Locate every Plasmodium falciparum-infected red blood cell.
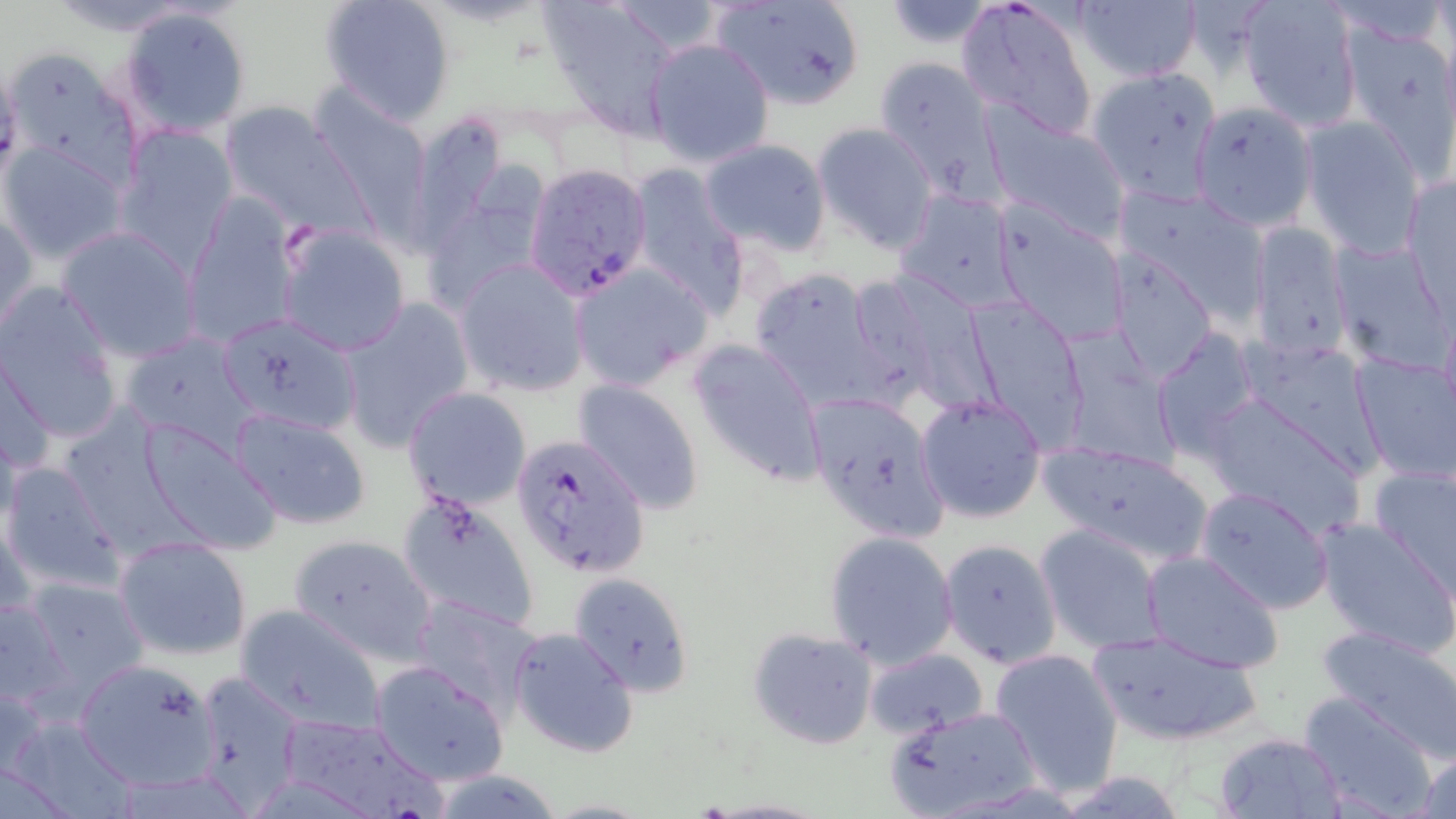
Approximate bounding boxes as (x1,y1)-(x2,y2) corner pairs in pixels.
Plasmodium falciparum-infected red blood cells: (524,163)-(655,300), (511,433)-(648,577).

{
  "slide_level_diagnosis": "Plasmodium falciparum",
  "magnification": "1000x",
  "stain": "May-Grünwald-Giemsa",
  "modality": "light microscopy",
  "field_of_view": "single",
  "uninfected_red_blood_cell_locations": "approximate bounding boxes as (x1,y1)-(x2,y2) corner pairs in pixels: (318,0)-(456,126), (538,0)-(682,138), (707,0)-(869,111), (957,0)-(1099,142), (1237,0)-(1363,132), (1074,1)-(1202,85), (883,2)-(998,49), (119,6)-(251,136), (1339,20)-(1453,169), (645,38)-(774,168), (874,56)-(1002,195), (1087,65)-(1220,206), (310,90)-(434,227), (1190,99)-(1316,231), (219,102)-(372,237), (399,108)-(510,256), (985,108)-(1131,242), (1299,117)-(1427,258), (812,123)-(937,252), (113,124)-(235,270), (699,138)-(832,255), (0,141)-(128,265), (428,153)-(539,300), (626,167)-(750,316), (1403,173)-(1455,307), (1114,185)-(1271,321), (895,190)-(1024,313), (182,197)-(303,348), (989,200)-(1130,345), (1,204)-(37,338), (1246,221)-(1352,364), (57,226)-(203,362), (277,226)-(410,355), (1330,237)-(1451,370), (1105,248)-(1219,383), (454,261)-(590,396), (572,262)-(713,390), (750,267)-(887,411), (847,270)-(1001,413), (1,281)-(125,445), (965,296)-(1089,449), (339,300)-(473,451), (217,312)-(363,434), (1153,328)-(1261,461), (121,332)-(258,449), (1061,336)-(1176,471), (688,338)-(827,486), (1242,341)-(1383,478), (0,345)-(55,481), (1351,351)-(1456,487), (573,379)-(704,513), (403,388)-(531,511), (1198,390)-(1368,533), (916,392)-(1047,524), (228,408)-(373,530), (822,409)-(946,544), (132,416)-(281,555), (1035,439)-(1219,568), (2,460)-(125,595), (1368,463)-(1455,596), (1194,486)-(1335,614), (395,489)-(540,632), (1313,517)-(1456,655), (1034,524)-(1170,653), (824,531)-(958,671), (289,532)-(438,663), (115,536)-(253,662), (939,539)-(1062,668), (1140,550)-(1283,675), (572,573)-(695,697), (18,575)-(153,704), (0,595)-(70,712), (411,596)-(544,721), (233,604)-(387,734), (1316,625)-(1456,763), (509,627)-(639,759), (747,628)-(879,750), (1085,630)-(1267,746), (989,647)-(1125,796), (865,648)-(989,738), (72,658)-(221,792), (370,660)-(510,787), (189,672)-(306,811), (0,676)-(48,782), (1298,693)-(1437,816), (884,706)-(1044,819), (277,712)-(441,819), (1213,732)-(1347,816), (1414,746)-(1456,818), (428,770)-(565,819)",
  "preparation": "thin blood film",
  "image_size": "1456×819 pixels"
}